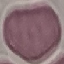

Malaria status: uninfected. Giemsa stain. Thin blood film. Automatically extracted cell patch, resized to 64 × 64 pixels. Acquired by smartphone through the microscope eyepiece.